Comment on the morphology of the red blood cells.
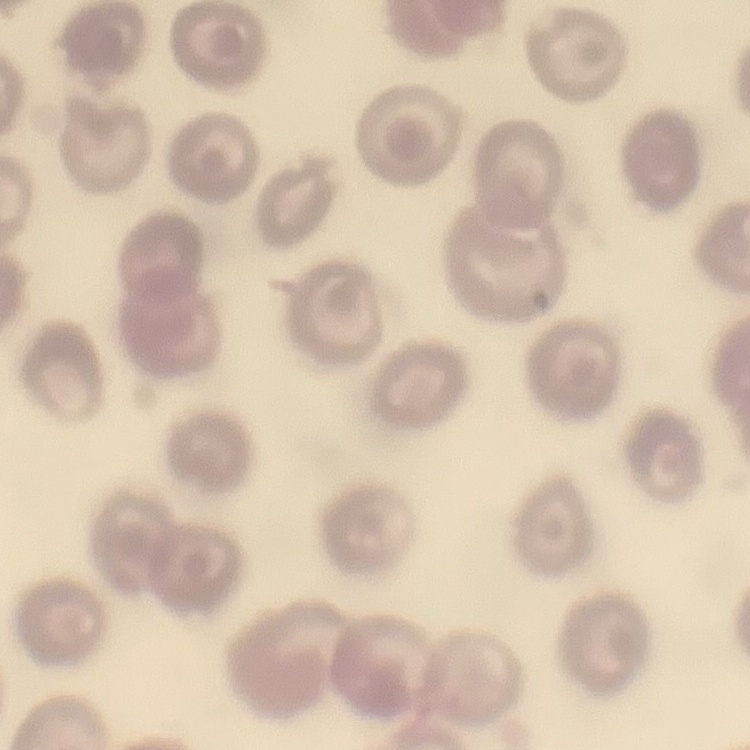

No rouleaux formation.

Summary:
  - Preparation: thin blood smear
  - Image type: square crop of a larger photomicrograph
  - Stain: Field's or Giemsa